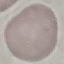
Summary:
  - Result: no malaria parasites detected
  - Preparation: thin smear
  - Stain: Giemsa
  - Image type: automatically extracted cell patch, resized to 64 × 64 pixels
  - Capture: smartphone through the microscope eyepiece